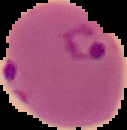

Image is 127×130 pixels. Malaria status: parasitized. From a thin blood smear. Cell region segmented out of the field of view; the surrounding area is masked to black.